Comment on the morphology of the red blood cells.
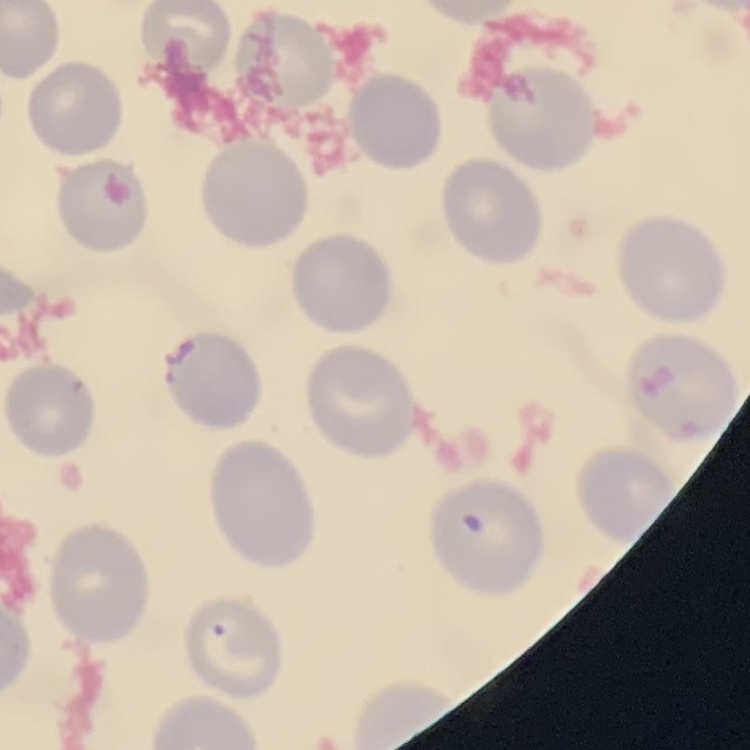
No rouleaux formation.

preparation = thin blood smear
image type = square crop of a larger photomicrograph
stain = Field's or Giemsa